Give the extent of all Plasmodium vivax-infected red blood cells.
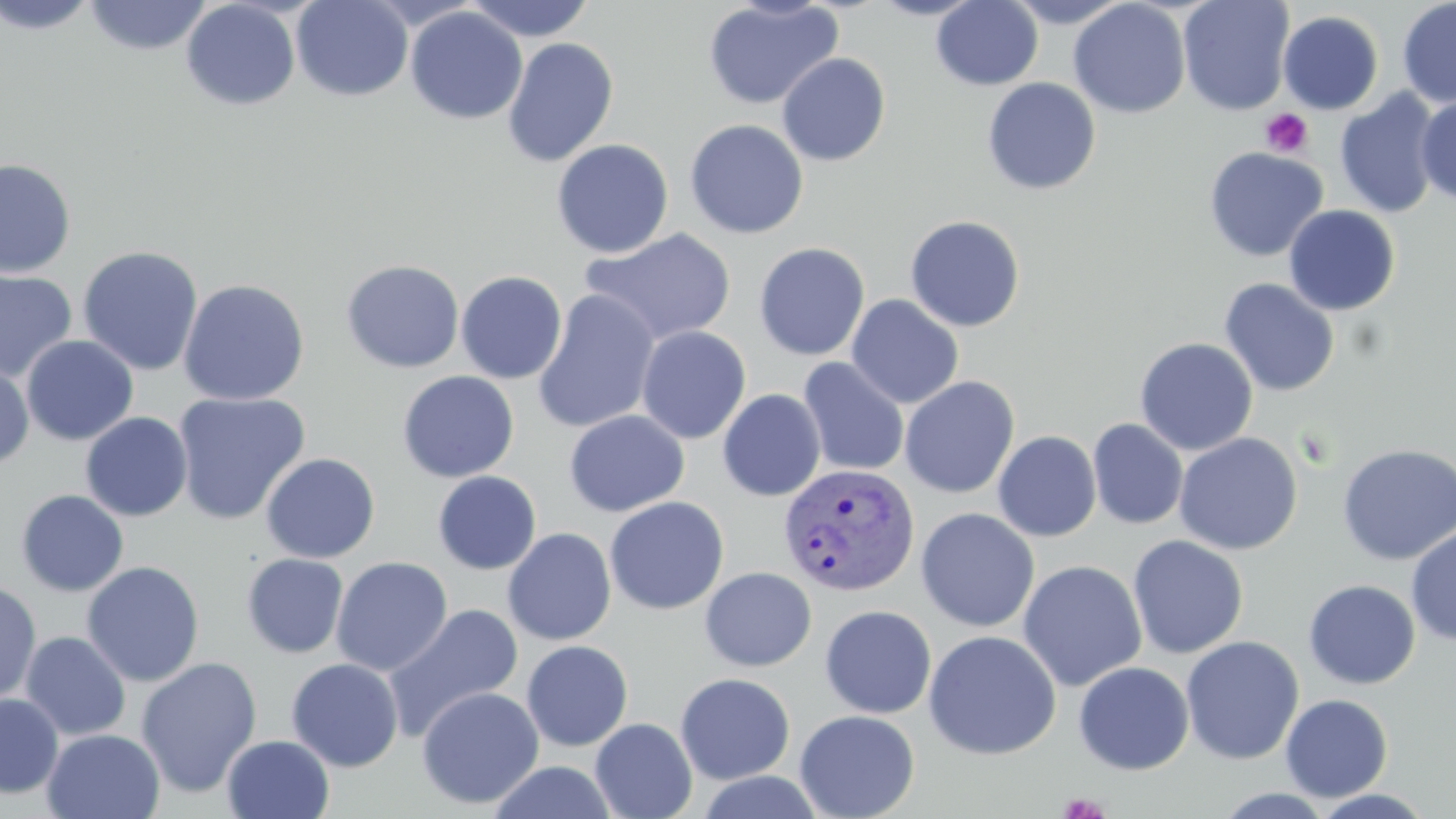
Approximate bounding boxes as named x1/y1/x2/y2 corners in pixels.
Plasmodium vivax-infected red blood cells: (x1=779, y1=463, x2=920, y2=596).

slide-level diagnosis = Plasmodium vivax
image size = 1456×819 pixels
stain = May-Grünwald-Giemsa
magnification = 1000x
uninfected red blood cell locations = approximate bounding boxes as named x1/y1/x2/y2 corners in pixels: (x1=0, y1=0, x2=101, y2=34), (x1=82, y1=0, x2=212, y2=56), (x1=291, y1=0, x2=414, y2=102), (x1=463, y1=0, x2=597, y2=42), (x1=867, y1=0, x2=986, y2=20), (x1=931, y1=0, x2=1043, y2=90), (x1=1000, y1=0, x2=1131, y2=28), (x1=1068, y1=0, x2=1191, y2=119), (x1=1177, y1=0, x2=1295, y2=116), (x1=1397, y1=0, x2=1456, y2=108), (x1=181, y1=1, x2=301, y2=110), (x1=702, y1=1, x2=843, y2=110), (x1=405, y1=6, x2=528, y2=124), (x1=1278, y1=10, x2=1383, y2=115), (x1=502, y1=37, x2=619, y2=167), (x1=776, y1=53, x2=891, y2=166), (x1=982, y1=77, x2=1101, y2=195), (x1=1334, y1=88, x2=1443, y2=218), (x1=1416, y1=95, x2=1456, y2=206), (x1=684, y1=119, x2=809, y2=239), (x1=552, y1=138, x2=674, y2=258), (x1=1203, y1=147, x2=1328, y2=262), (x1=0, y1=158, x2=77, y2=278), (x1=1283, y1=205, x2=1401, y2=315), (x1=904, y1=214, x2=1026, y2=332), (x1=579, y1=227, x2=737, y2=346), (x1=754, y1=242, x2=870, y2=361), (x1=78, y1=245, x2=204, y2=376), (x1=341, y1=259, x2=465, y2=373), (x1=0, y1=269, x2=78, y2=383), (x1=456, y1=270, x2=568, y2=384), (x1=178, y1=278, x2=310, y2=406), (x1=1219, y1=278, x2=1339, y2=397), (x1=532, y1=289, x2=661, y2=434), (x1=846, y1=294, x2=964, y2=408), (x1=636, y1=325, x2=751, y2=444), (x1=21, y1=334, x2=139, y2=446), (x1=1134, y1=337, x2=1259, y2=456), (x1=798, y1=357, x2=909, y2=476), (x1=0, y1=362, x2=34, y2=469), (x1=397, y1=370, x2=519, y2=482), (x1=900, y1=376, x2=1019, y2=498), (x1=717, y1=389, x2=826, y2=502), (x1=173, y1=391, x2=310, y2=525), (x1=564, y1=409, x2=689, y2=517), (x1=80, y1=412, x2=193, y2=522), (x1=1088, y1=418, x2=1188, y2=530), (x1=993, y1=430, x2=1102, y2=541), (x1=1174, y1=432, x2=1303, y2=555), (x1=1337, y1=442, x2=1456, y2=566), (x1=261, y1=452, x2=380, y2=563), (x1=432, y1=470, x2=542, y2=575), (x1=16, y1=489, x2=129, y2=597), (x1=604, y1=496, x2=729, y2=615), (x1=916, y1=507, x2=1040, y2=632), (x1=1406, y1=525, x2=1456, y2=647), (x1=502, y1=527, x2=617, y2=645), (x1=1128, y1=535, x2=1249, y2=659), (x1=242, y1=553, x2=349, y2=658), (x1=331, y1=556, x2=453, y2=676), (x1=1018, y1=559, x2=1147, y2=692), (x1=82, y1=561, x2=205, y2=687), (x1=692, y1=567, x2=807, y2=787), (x1=699, y1=567, x2=817, y2=672), (x1=0, y1=579, x2=42, y2=706), (x1=1303, y1=579, x2=1421, y2=689), (x1=384, y1=603, x2=524, y2=740), (x1=819, y1=605, x2=937, y2=718), (x1=924, y1=629, x2=1061, y2=759), (x1=20, y1=631, x2=131, y2=741), (x1=1181, y1=635, x2=1304, y2=765), (x1=521, y1=640, x2=634, y2=751), (x1=136, y1=656, x2=262, y2=798), (x1=286, y1=658, x2=404, y2=771), (x1=1073, y1=661, x2=1194, y2=775), (x1=674, y1=672, x2=796, y2=784), (x1=416, y1=686, x2=544, y2=809), (x1=0, y1=693, x2=64, y2=799), (x1=1280, y1=693, x2=1393, y2=802), (x1=794, y1=709, x2=920, y2=819), (x1=590, y1=717, x2=697, y2=819), (x1=42, y1=729, x2=165, y2=818), (x1=221, y1=734, x2=335, y2=819), (x1=486, y1=760, x2=620, y2=818), (x1=1214, y1=788, x2=1337, y2=818), (x1=1310, y1=789, x2=1436, y2=818)
platelet locations = approximate bounding boxes as named x1/y1/x2/y2 corners in pixels: (x1=1260, y1=108, x2=1313, y2=158), (x1=1059, y1=793, x2=1109, y2=818)
preparation = thin blood film
field of view = single
modality = light microscopy